Assess this cell for malaria.
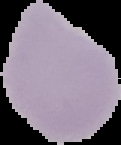
Uninfected.

image size = 121×145 pixels
image type = segmented cell region with the area outside set to black
preparation = thin blood film